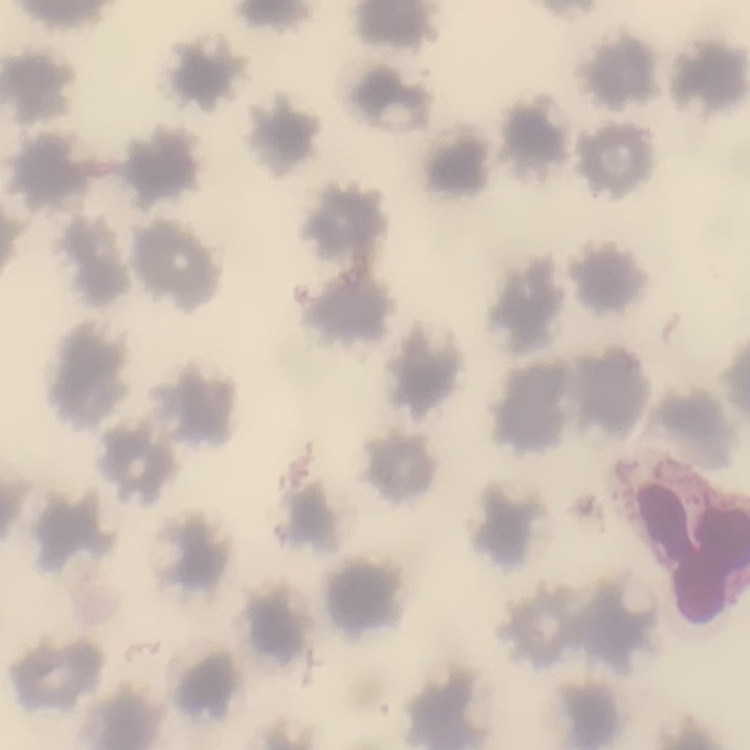 The red blood cells exhibit no rouleaux formation. Stained with either Field's or Giemsa. Thin peripheral smear. Square crop of a larger photomicrograph.